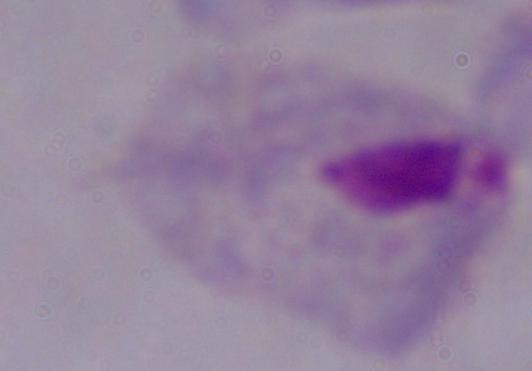

identification = trichomonad
magnification = 1000x
modality = photomicrograph